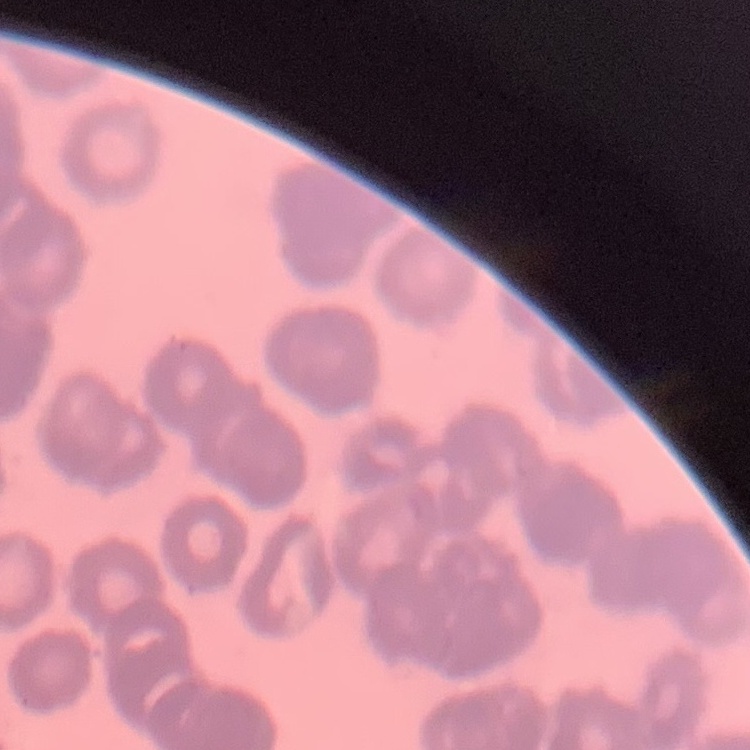

red blood cell morphology = rouleaux formation
stain = Field's or Giemsa
preparation = thin blood smear
image type = square crop of a larger photomicrograph